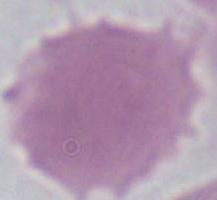
Photomicrograph. 1000x magnification. A red blood cell is shown.